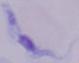

1000x magnification. Micrograph. A trypanosome is shown.